Assess this cell for malaria.
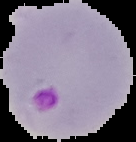
Parasitized.

From a thin blood film. Cell region segmented out of the field of view; the surrounding area is masked to black. Image is 136×142 pixels.